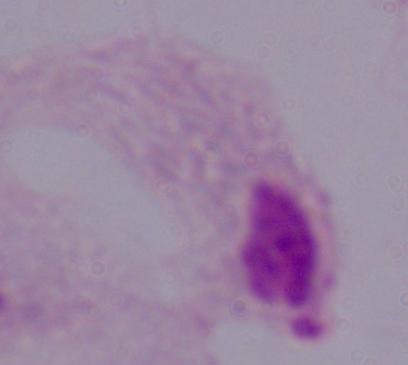

modality: micrograph
magnification: 1000x
identification: trichomonad